Point out each malaria parasite and each leukocyte.
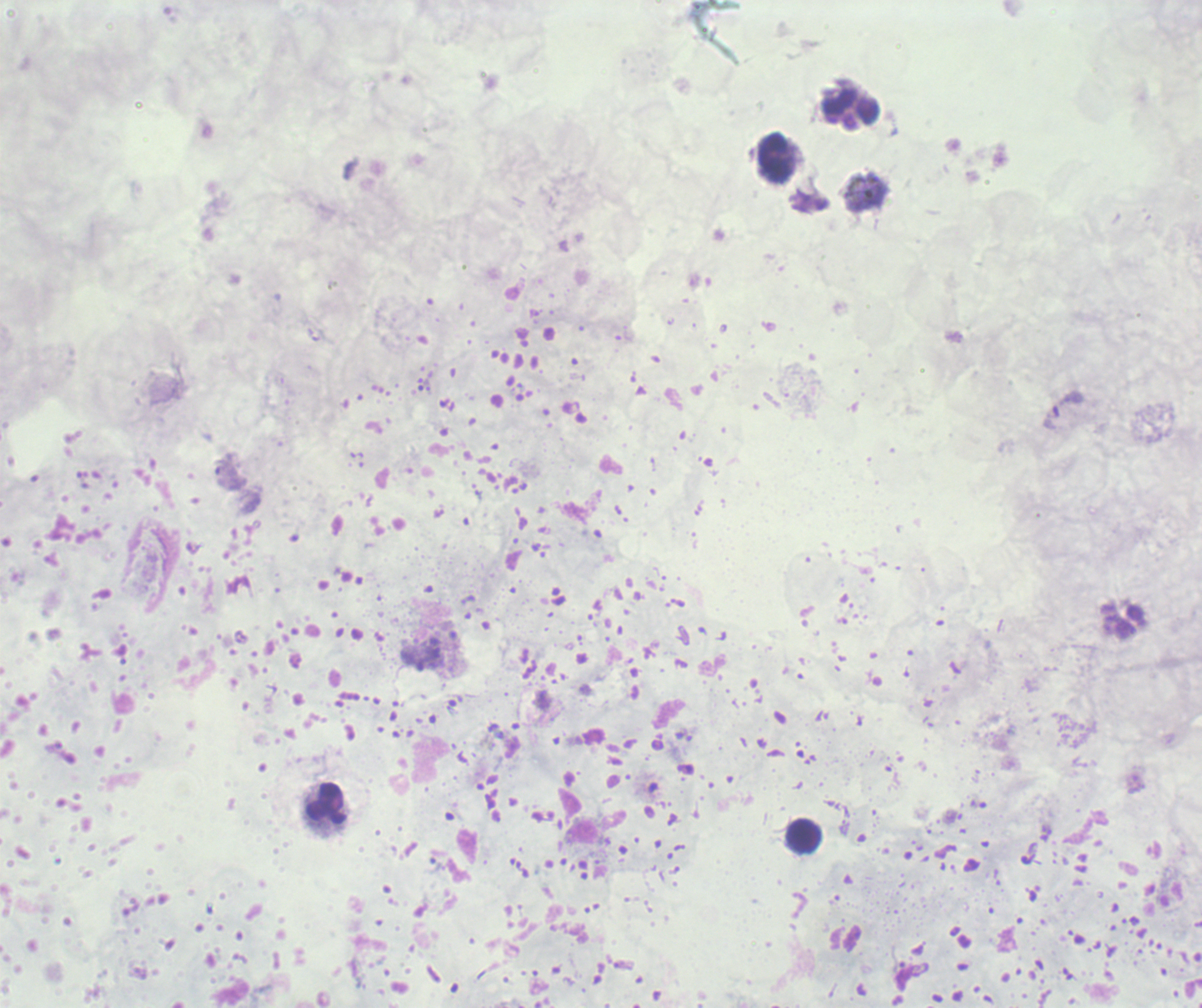

Negative for malaria parasites.
Approximate centers as {x, y} in pixels.
Leukocytes: {851, 109}, {775, 158}, {326, 804}, {803, 835}.

stain = Romanowsky
context = previously used in a real diagnosis
background quality = unsatisfactory
magnification = 100x
image size = 1202×1008 pixels
field of view = one from this slide
preparation = thick blood film